Assess this cell for malaria.
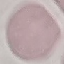

It is uninfected.

Summary:
  - Stain: Giemsa
  - Capture: smartphone through the microscope eyepiece
  - Image type: cell patch, automatically extracted from a larger field of view and resized to 64 × 64 pixels
  - Preparation: thin blood smear